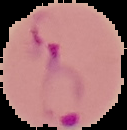
Summary:
  - Image type: cell region segmented out of the field of view; surrounding area masked to black
  - Result: malaria parasites identified
  - Preparation: thin blood smear
  - Image size: 127×130 pixels